Identify the parasite.
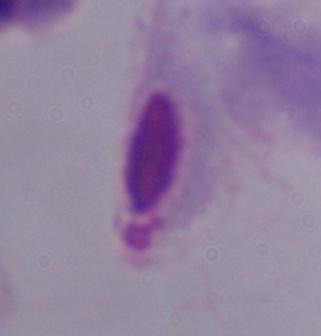

This is a trichomonad.

Summary:
  - Modality: micrograph
  - Magnification: 1000x